Name the blood parasite species.
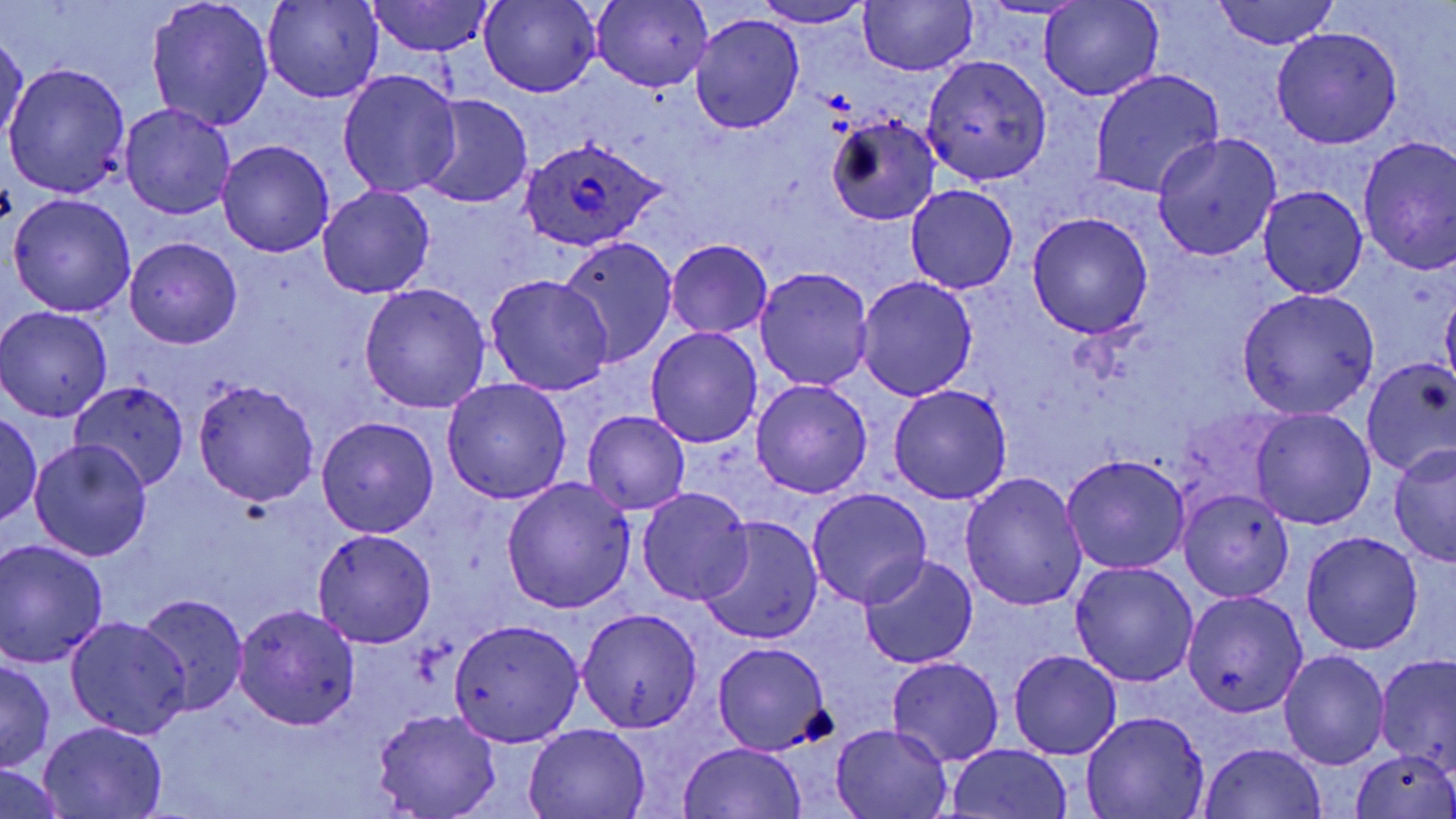
Plasmodium ovale.

Summary:
  - Coordinate format: approximate bounding boxes as (x1,y1)-(x2,y2) corner pairs in pixels
  - Uninfected red blood cell locations: (261,0)-(383,105), (365,0)-(493,55), (860,0)-(976,75), (1039,0)-(1162,100), (1213,0)-(1338,49), (146,1)-(273,131), (479,1)-(599,97), (591,1)-(712,91), (755,1)-(874,28), (691,13)-(805,134), (1271,27)-(1401,149), (2,29)-(30,144), (921,53)-(1053,185), (3,60)-(130,197), (338,69)-(461,198), (1090,70)-(1224,198), (417,95)-(534,209), (120,103)-(235,218), (827,113)-(941,226), (1152,132)-(1281,261), (1357,135)-(1456,273), (217,141)-(333,256), (904,184)-(1019,294), (317,185)-(435,298), (1259,186)-(1368,297), (8,194)-(136,318), (1026,212)-(1153,338), (125,237)-(242,349), (556,239)-(676,366), (666,239)-(772,339), (756,267)-(873,391), (487,274)-(611,393), (855,276)-(978,401), (359,283)-(490,413), (1236,288)-(1381,419), (1441,288)-(1456,389), (0,307)-(113,423), (645,326)-(763,448), (1361,359)-(1456,477), (193,378)-(320,506), (442,378)-(571,506), (751,379)-(872,499), (73,381)-(191,490), (887,384)-(1012,506), (1250,407)-(1376,530), (581,410)-(692,515), (0,413)-(43,524), (316,416)-(439,538), (30,440)-(152,561), (1388,445)-(1456,568), (1062,453)-(1190,574), (960,473)-(1087,613), (503,478)-(634,613), (637,487)-(754,605), (806,488)-(932,610), (1178,489)-(1294,603), (695,517)-(822,644), (312,528)-(437,647), (1300,530)-(1423,654), (0,541)-(109,667), (860,555)-(978,672), (1069,561)-(1199,688), (138,592)-(249,715), (1182,592)-(1307,718), (233,604)-(362,731), (576,609)-(702,732), (66,614)-(190,739), (448,618)-(585,747), (712,642)-(831,755), (1279,649)-(1389,770), (1009,650)-(1121,759), (1376,655)-(1455,776), (0,657)-(55,772), (886,658)-(1004,768), (372,707)-(501,819), (1082,712)-(1207,819), (38,721)-(167,817), (523,725)-(652,818), (833,725)-(953,817), (677,742)-(808,819), (1201,742)-(1326,818), (946,743)-(1073,818), (1350,750)-(1456,819), (0,766)-(70,817)
  - Plasmodium ovale-infected red blood cell locations: (520,138)-(668,252)
  - Modality: optical microscopy
  - Stain: May-Grünwald-Giemsa
  - Image size: 1456×819 pixels
  - Preparation: thin blood smear
  - Field of view: one of a larger specimen
  - Magnification: 1000x